Report the malaria status of this cell.
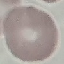
It is uninfected.

Thin blood smear. Photographed with a smartphone camera at the microscope eyepiece. Giemsa stain. Automatically extracted cell patch, resized to 64 × 64 pixels.